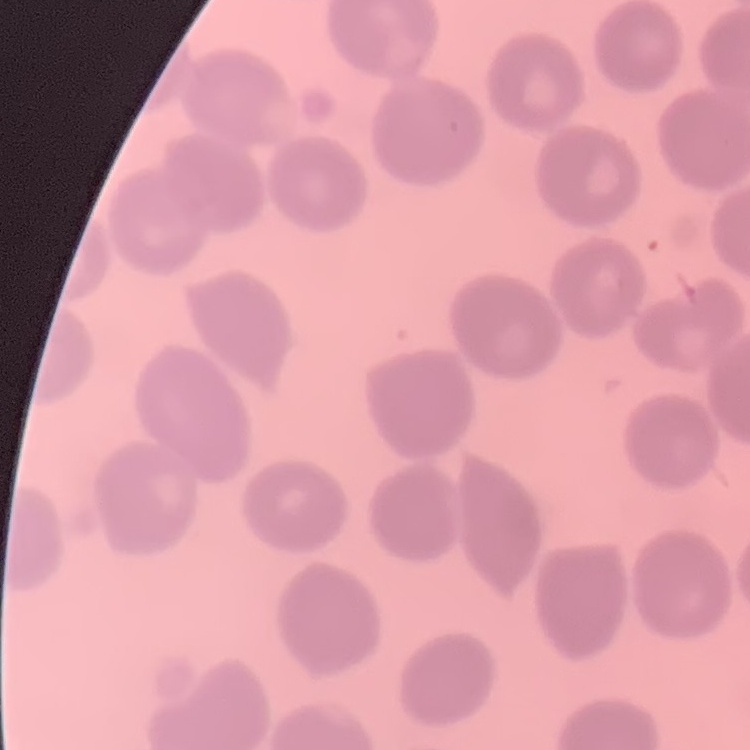

Summary:
  - Red blood cell morphology: no rouleaux formation
  - Image type: square crop of a larger photomicrograph
  - Preparation: thin peripheral smear
  - Stain: Field's or Giemsa